Describe the morphology of the red blood cells.
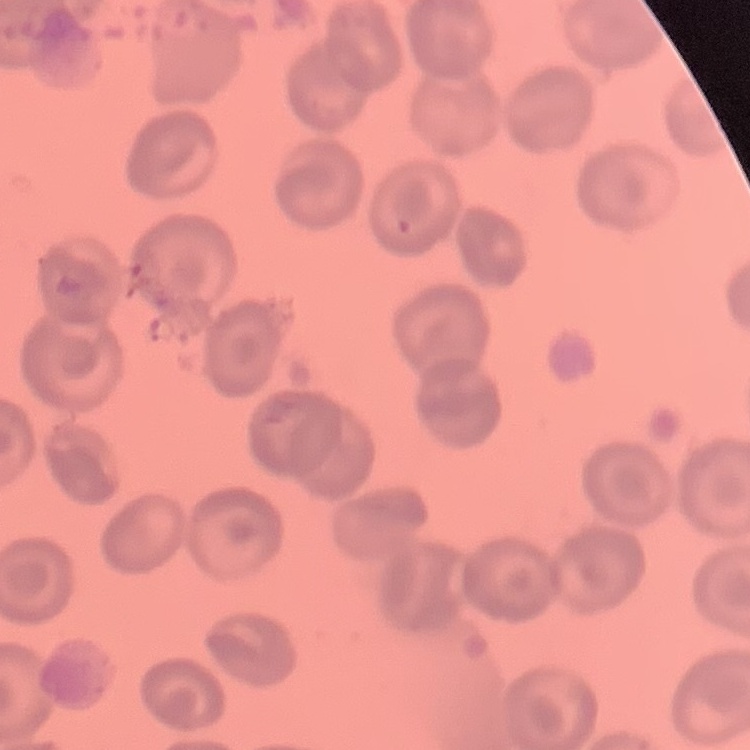

No rouleaux formation.

Stained with either Field's or Giemsa. One tile cut from a larger photomicrograph. Thin peripheral smear.